Report the malaria status of this cell.
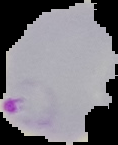
Parasitized.

image size = 118×145 pixels
preparation = thin blood smear
image type = segmented cell region on a black background